Identify the parasite.
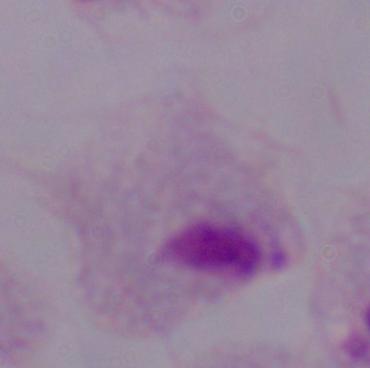
A trichomonad.

Photomicrograph. 1000x magnification.